Identify the cell.
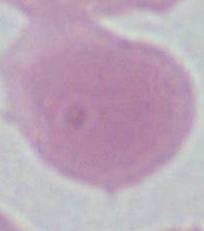

This is an erythrocyte.

Summary:
  - Modality: micrograph
  - Magnification: 1000x